Locate every uninfected red blood cell.
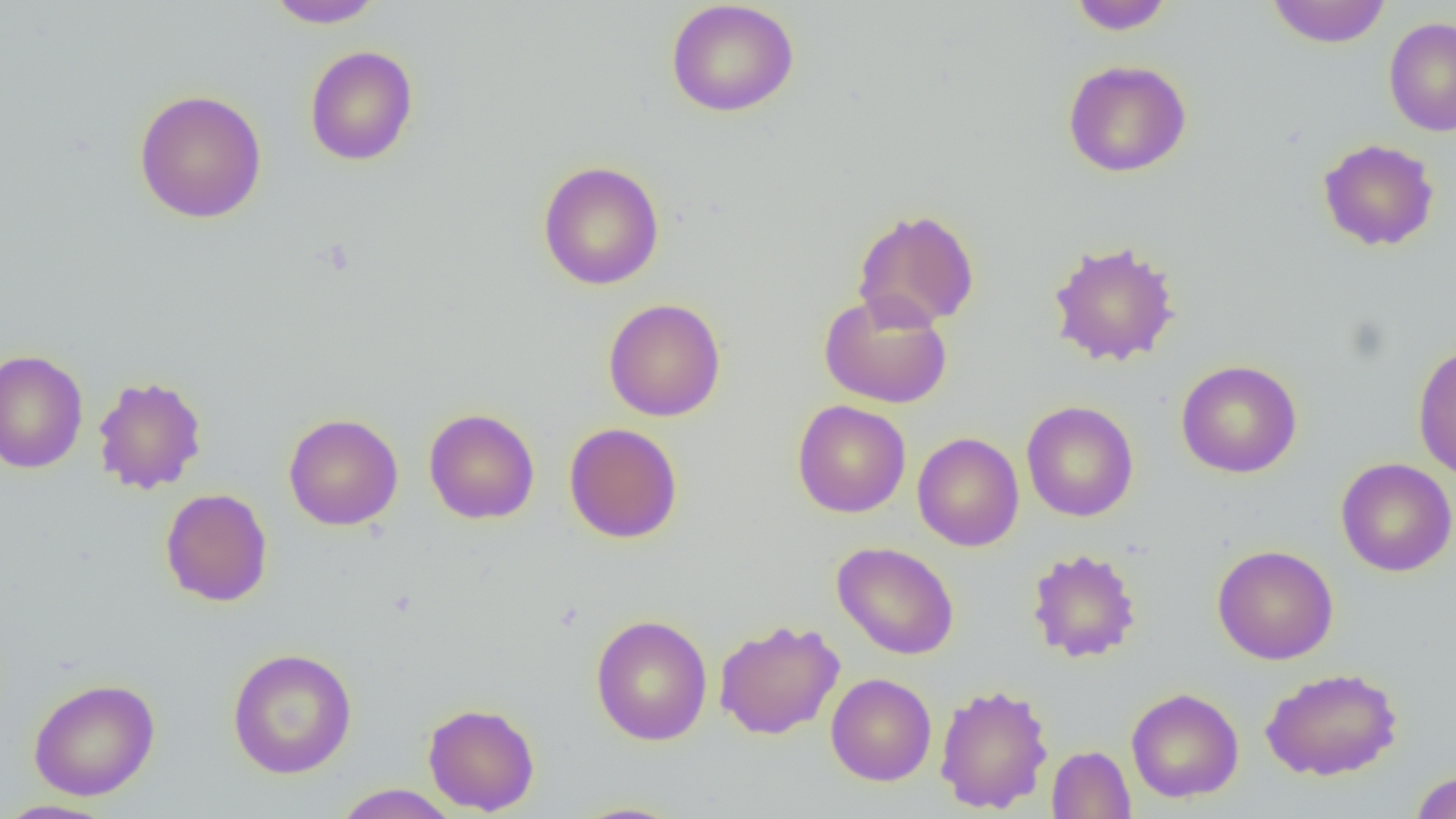

Approximate bounding boxes as (x1, y1, x2, y2) in pixels.
Uninfected red blood cells: (265, 0, 386, 29), (665, 0, 800, 118), (1068, 0, 1175, 35), (1266, 0, 1391, 48), (1384, 16, 1456, 137), (304, 45, 418, 166), (1063, 59, 1192, 178), (133, 88, 268, 223), (1317, 138, 1440, 252), (538, 160, 665, 291), (852, 208, 980, 331), (1046, 239, 1182, 367), (818, 292, 953, 409), (603, 298, 726, 422), (1412, 342, 1456, 481), (0, 349, 88, 474), (1176, 359, 1303, 479), (92, 375, 208, 495), (792, 400, 911, 518), (1022, 401, 1138, 522), (424, 408, 540, 524), (283, 413, 403, 531), (563, 422, 683, 544), (912, 432, 1025, 551), (1336, 458, 1456, 577), (160, 488, 273, 606), (831, 541, 960, 660), (1212, 544, 1339, 665), (1026, 547, 1142, 663), (591, 614, 713, 746), (713, 619, 845, 740), (227, 647, 358, 779), (1260, 667, 1403, 781), (825, 673, 937, 786), (28, 678, 160, 800), (934, 682, 1054, 814), (1126, 687, 1244, 803), (423, 702, 539, 815), (1047, 745, 1136, 818), (1410, 770, 1456, 819), (332, 784, 461, 818), (0, 799, 118, 818).

Summary:
  - Slide-level diagnosis: no evidence of blood parasites
  - Modality: light microscopy
  - Preparation: thin blood smear
  - Field of view: one of a larger specimen
  - Magnification: 1000x
  - Image size: 1456×819 pixels